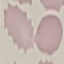
Summary:
  - Malaria status: uninfected
  - Preparation: thin blood film
  - Capture: smartphone camera at the microscope eyepiece
  - Stain: Giemsa
  - Image type: automatically extracted cell patch, resized to 64 × 64 pixels